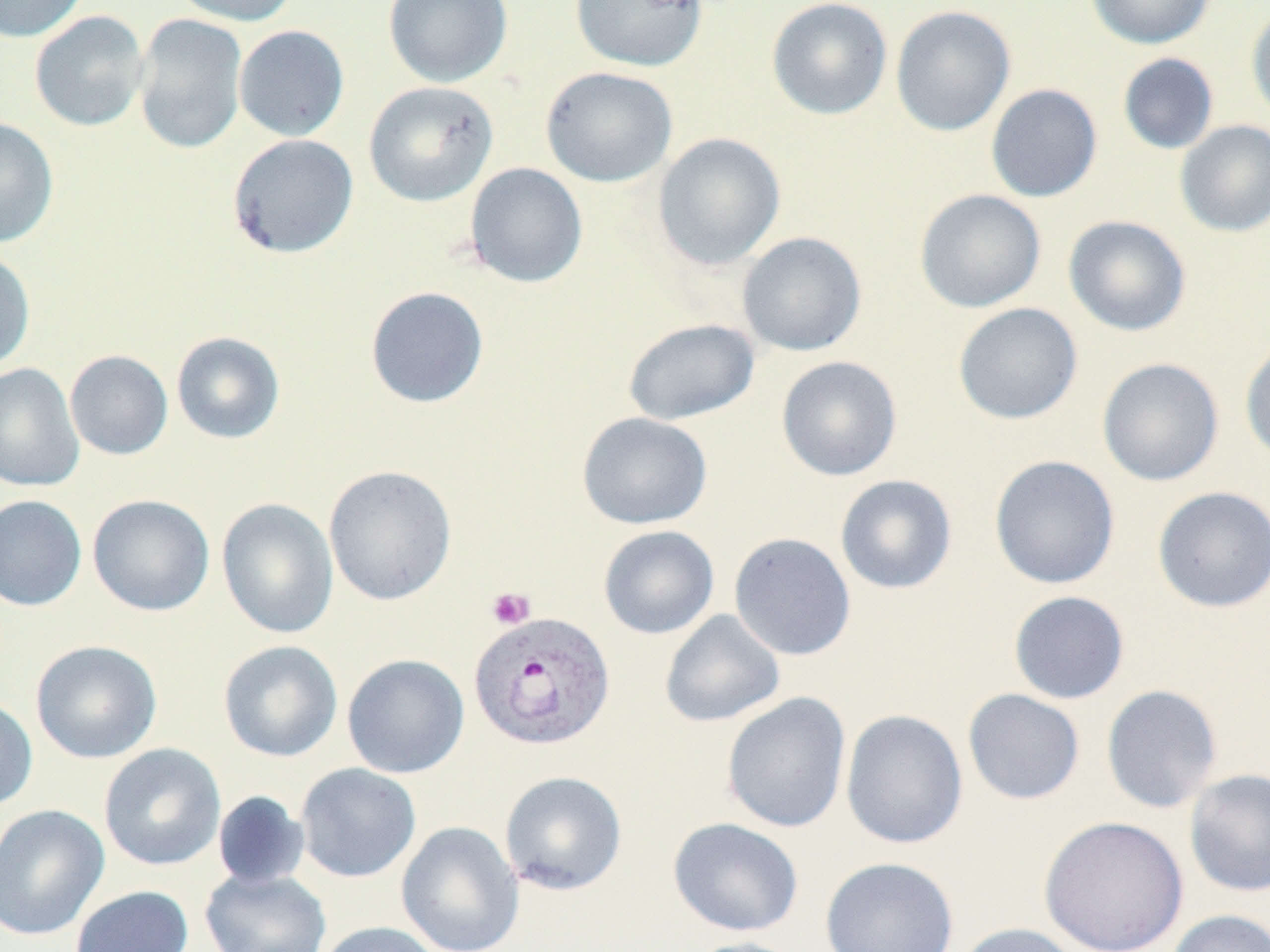
slide-level diagnosis = Plasmodium vivax
magnification = 1000x
platelet locations = approximate bounding boxes as [x1, y1, x2, y2] in pixels: [486, 586, 535, 629]
field of view = one of a larger specimen
uninfected red blood cell locations = approximate bounding boxes as [x1, y1, x2, y2] in pixels: [0, 0, 88, 42], [169, 0, 298, 26], [382, 0, 513, 88], [570, 0, 708, 71], [766, 0, 893, 120], [1086, 0, 1215, 49], [890, 5, 1016, 136], [1246, 6, 1270, 125], [29, 11, 149, 131], [133, 13, 247, 154], [234, 25, 350, 141], [1117, 53, 1219, 155], [541, 66, 678, 187], [363, 81, 498, 206], [985, 84, 1103, 202], [0, 117, 59, 248], [1174, 120, 1270, 237], [652, 132, 786, 270], [227, 133, 358, 258], [465, 162, 588, 288], [914, 188, 1046, 312], [1063, 215, 1191, 337], [736, 231, 867, 356], [0, 249, 36, 372], [365, 286, 489, 409], [953, 302, 1083, 425], [622, 318, 760, 426], [171, 331, 285, 444], [1239, 336, 1270, 465], [65, 350, 173, 460], [776, 356, 902, 481], [1097, 357, 1225, 487], [0, 362, 85, 492], [577, 412, 713, 529], [989, 455, 1120, 590], [323, 464, 457, 606], [835, 474, 957, 594], [1152, 486, 1270, 613], [0, 494, 87, 612], [87, 494, 215, 616], [217, 497, 339, 639], [598, 525, 719, 639], [729, 532, 856, 660], [1008, 590, 1130, 704], [660, 609, 785, 727], [30, 640, 162, 763], [218, 640, 343, 761], [342, 653, 469, 778], [1101, 683, 1223, 814], [962, 688, 1085, 805], [721, 691, 852, 834], [0, 695, 38, 811], [840, 709, 968, 850], [98, 743, 226, 871], [295, 763, 421, 882], [1184, 767, 1270, 897], [499, 771, 628, 895], [212, 790, 310, 890], [0, 803, 110, 941], [1038, 815, 1189, 952], [668, 817, 804, 937], [396, 821, 524, 952], [819, 856, 959, 952], [200, 867, 331, 952], [70, 885, 194, 952], [1164, 908, 1270, 952], [313, 920, 444, 952], [952, 922, 1086, 952], [681, 937, 809, 952]
image size = 1270×952 pixels
preparation = thin blood smear
Plasmodium vivax-infected red blood cell locations = approximate bounding boxes as [x1, y1, x2, y2] in pixels: [468, 609, 616, 751]
stain = May-Grünwald-Giemsa
modality = optical microscopy